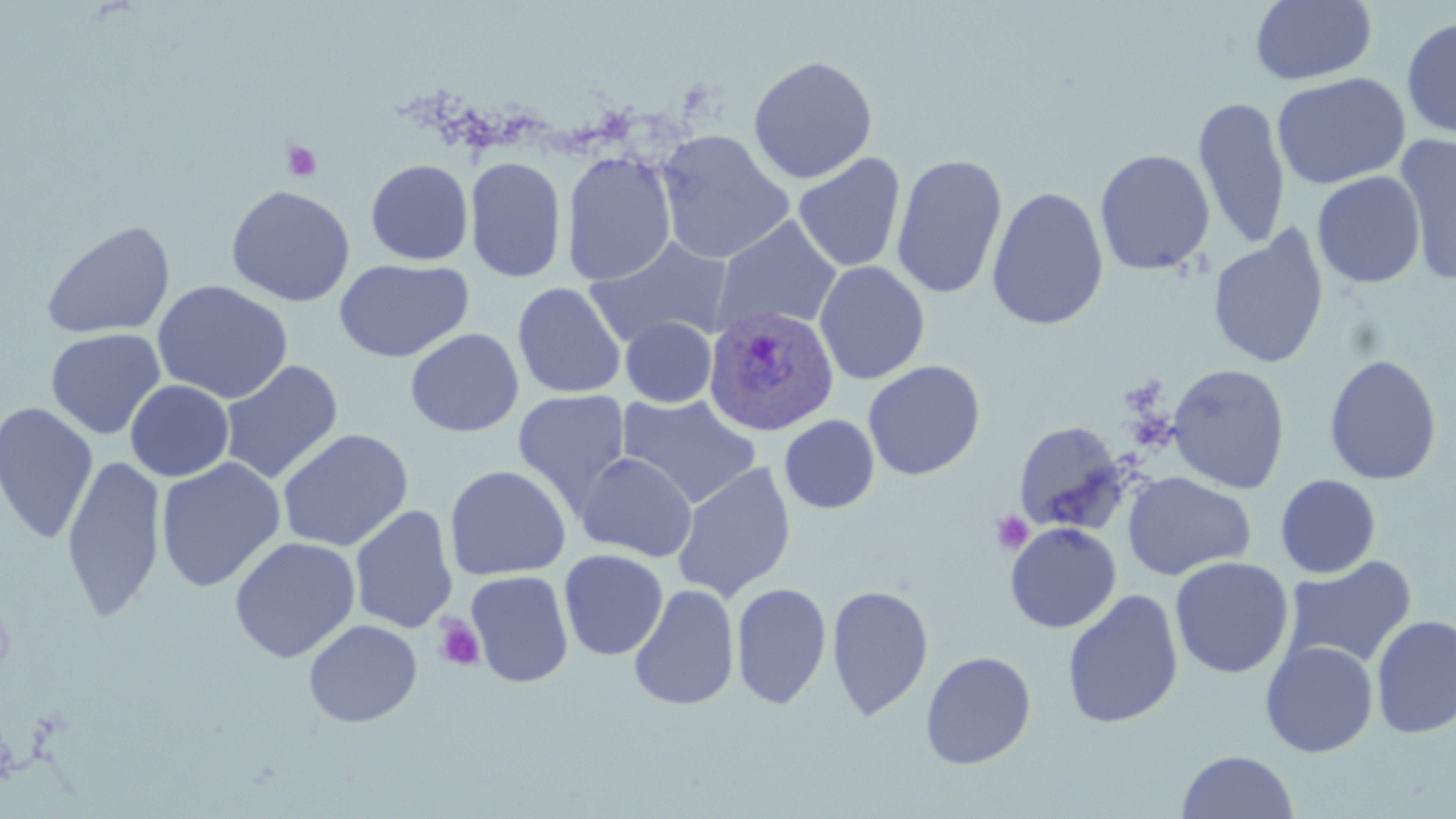

Approximate bounding boxes as [x1, y1, x2, y2] in pixels. Platelet locations: [281, 140, 323, 183], [990, 511, 1034, 555], [433, 615, 486, 672]. Uninfected red blood cell locations: [1250, 0, 1377, 86], [1401, 14, 1456, 139], [748, 55, 878, 184], [1272, 72, 1411, 190], [1194, 97, 1291, 251], [655, 129, 795, 265], [1394, 134, 1456, 282], [1094, 148, 1215, 276], [561, 150, 677, 286], [793, 152, 906, 272], [891, 153, 1008, 300], [465, 155, 567, 283], [365, 158, 473, 265], [1312, 171, 1426, 288], [226, 185, 355, 306], [987, 186, 1109, 331], [712, 216, 842, 333], [40, 219, 176, 341], [1208, 226, 1330, 369], [585, 236, 733, 348], [334, 258, 473, 363], [813, 261, 930, 384], [152, 279, 294, 404], [512, 282, 627, 399], [621, 316, 716, 407], [45, 328, 166, 440], [405, 328, 524, 437], [1323, 354, 1442, 486], [218, 359, 344, 484], [863, 360, 986, 481], [1167, 363, 1290, 494], [124, 380, 234, 482], [512, 390, 631, 514], [618, 393, 761, 509], [0, 401, 99, 544], [779, 415, 879, 513], [1013, 419, 1130, 534], [276, 428, 414, 552], [575, 451, 698, 562], [61, 454, 166, 623], [155, 456, 286, 591], [671, 461, 797, 603], [444, 464, 571, 580], [1122, 471, 1255, 580], [1275, 474, 1381, 578], [349, 505, 458, 634], [1004, 522, 1121, 633], [229, 536, 361, 663], [559, 549, 669, 660], [1170, 556, 1294, 679], [1282, 556, 1417, 671], [465, 570, 574, 688], [731, 582, 832, 710], [827, 582, 933, 722], [628, 584, 740, 711], [1062, 590, 1184, 729], [1371, 614, 1456, 739], [303, 619, 423, 727], [1261, 641, 1379, 758], [920, 651, 1037, 769], [1176, 750, 1299, 818]. Plasmodium ovale-infected red blood cell locations: [703, 304, 839, 436]. Slide-level diagnosis: Plasmodium ovale. May-Grünwald-Giemsa stain. 1000x magnification. Light microscopy. Thin blood film. Image is 1456×819 pixels. Single field of view.